Assess this cell for malaria.
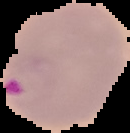

It is parasitized.

Summary:
  - Preparation: thin blood film
  - Image size: 130×133 pixels
  - Image type: segmented cell region with the area outside set to black